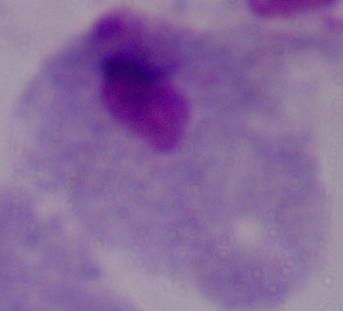
Summary:
  - Identification: trichomonad
  - Magnification: 1000x
  - Modality: photomicrograph